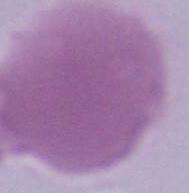

identification = red blood cell
modality = photomicrograph
magnification = 1000x